State which cell type is depicted.
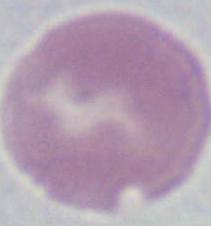

This is an erythrocyte.

modality: micrograph
magnification: 1000x